Comment on the morphology of the erythrocytes.
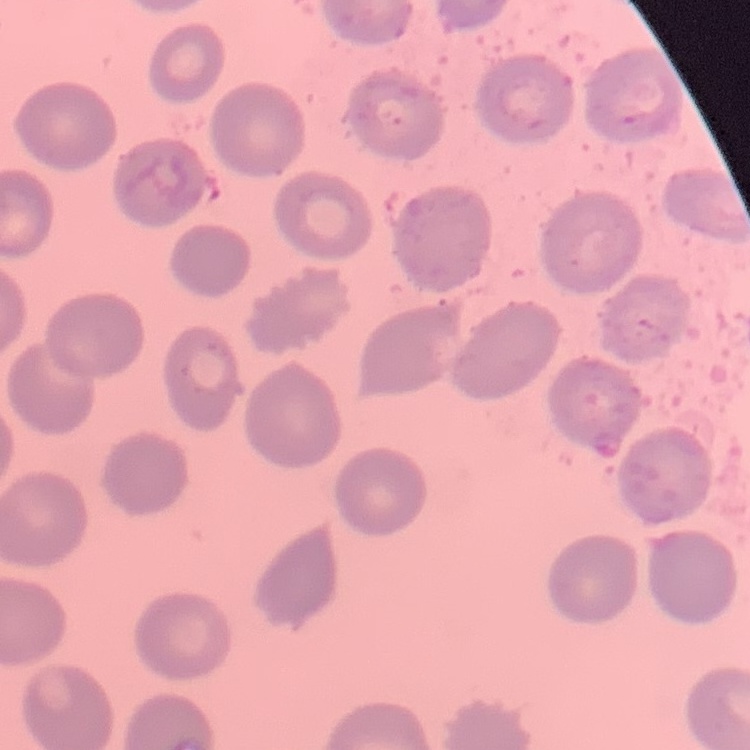
They show no rouleaux formation.

Stained with either Field's or Giemsa. Thin peripheral smear. One tile cut from a larger photomicrograph.